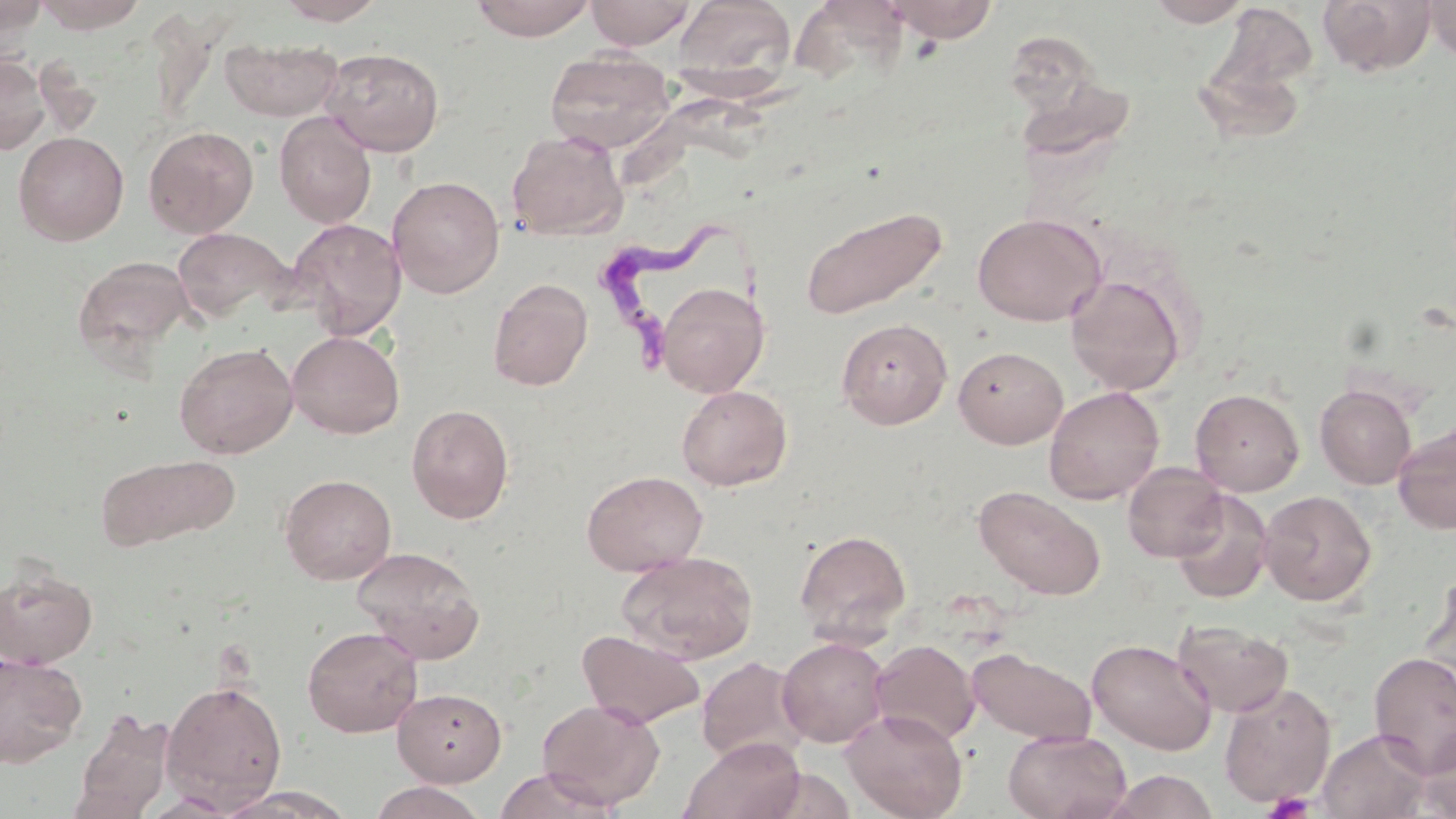

Summary:
  - Coordinate format: approximate bounding boxes as [x1, y1, x2, y2] in pixels
  - Uninfected red blood cell locations: [34, 0, 149, 33], [275, 0, 388, 25], [470, 0, 595, 41], [585, 0, 696, 49], [672, 0, 797, 91], [884, 0, 1000, 43], [1146, 0, 1254, 27], [1317, 0, 1437, 76], [1424, 0, 1456, 61], [0, 1, 49, 42], [1214, 3, 1320, 95], [220, 37, 344, 122], [321, 47, 445, 157], [545, 50, 675, 154], [0, 54, 50, 155], [274, 112, 377, 228], [143, 125, 259, 238], [507, 129, 628, 241], [13, 131, 129, 246], [388, 176, 505, 299], [799, 204, 949, 321], [972, 213, 1106, 326], [287, 218, 407, 340], [170, 226, 294, 327], [72, 254, 195, 364], [1065, 274, 1186, 396], [488, 278, 593, 391], [656, 281, 770, 397], [836, 318, 952, 429], [287, 331, 405, 438], [174, 342, 298, 459], [954, 345, 1068, 448], [1315, 383, 1417, 489], [676, 385, 792, 491], [1044, 386, 1164, 505], [1190, 388, 1305, 496], [406, 404, 514, 523], [1392, 421, 1456, 536], [97, 453, 239, 551], [1122, 462, 1229, 563], [581, 470, 708, 575], [280, 474, 397, 584], [974, 485, 1106, 600], [1171, 490, 1274, 604], [1259, 490, 1377, 606], [794, 529, 912, 644], [351, 546, 486, 663], [616, 551, 758, 665], [0, 561, 99, 669], [1173, 620, 1294, 717], [301, 625, 423, 737], [577, 630, 705, 729], [777, 637, 890, 747], [1086, 638, 1217, 755], [870, 639, 980, 746], [967, 647, 1097, 746], [1368, 651, 1456, 778], [0, 652, 87, 767], [696, 655, 809, 767], [161, 678, 288, 811], [1219, 682, 1336, 808], [393, 687, 508, 785], [536, 699, 665, 810], [70, 708, 175, 819], [841, 708, 968, 819], [1413, 725, 1456, 818], [1317, 728, 1434, 818], [1003, 729, 1131, 819], [682, 736, 806, 819], [493, 767, 616, 819], [1103, 770, 1220, 819], [368, 781, 489, 819], [212, 786, 356, 819], [140, 792, 242, 817]
  - Platelet locations: [1262, 790, 1315, 818]
  - Trypanosoma brucei locations: [599, 212, 747, 380]
  - Slide-level diagnosis: Trypanosoma brucei
  - Modality: light microscopy
  - Field of view: one of a larger specimen
  - Stain: May-Grünwald-Giemsa
  - Image size: 1456×819 pixels
  - Magnification: 1000x
  - Preparation: thin blood film